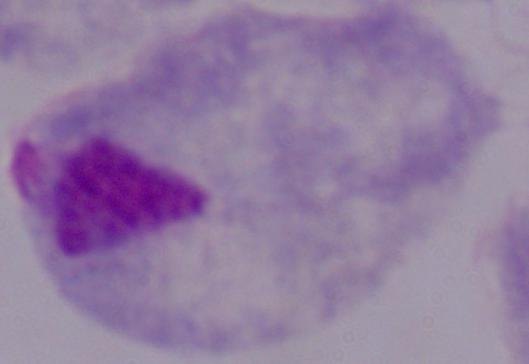

A trichomonad is seen. Micrograph. 1000x magnification.